Assess the morphology of the erythrocytes.
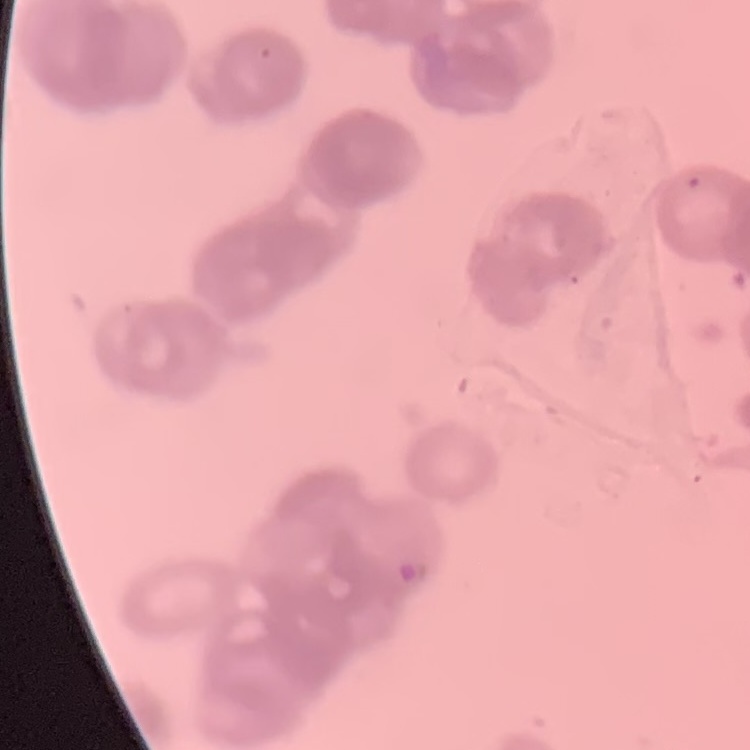
They show rouleaux formation.

Summary:
  - Image type: one tile cut from a larger photomicrograph
  - Stain: Field's or Giemsa
  - Preparation: thin peripheral smear